Mark where leukocytes are.
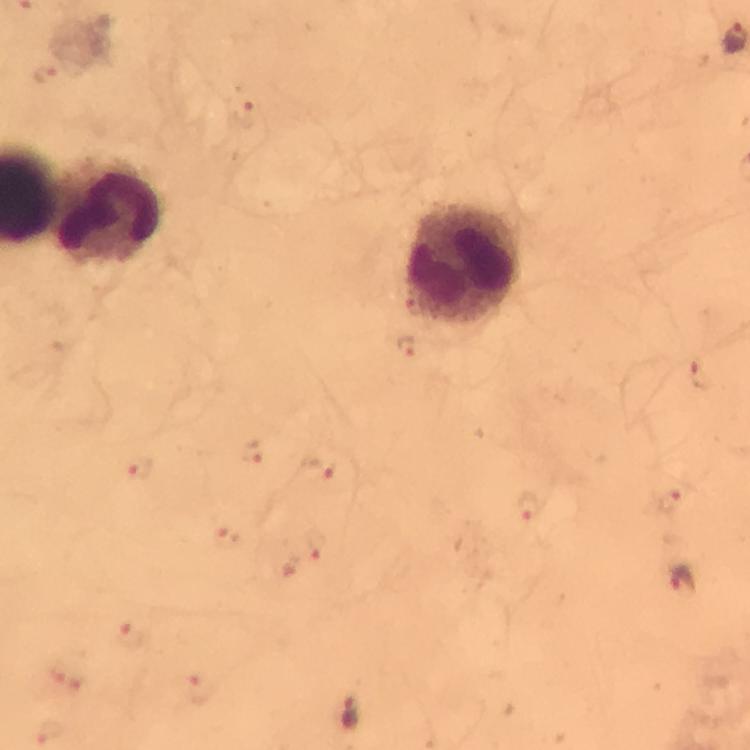
Approximate centers as {x, y} in pixels.
Leukocytes: {107, 211}, {466, 261}.

Malaria parasite locations: {47, 72}, {242, 114}, {406, 345}, {700, 375}, {253, 454}, {318, 469}, {139, 472}, {670, 502}, {528, 507}, {226, 537}, {317, 545}, {685, 580}, {131, 635}, {200, 689}, {351, 713}, {52, 732}. From a malaria diagnostic workup. Photographed through the microscope with a smartphone camera. Image is 750×750 pixels. 100x magnification. Thick blood film. Immersion oil was used. Cropped region of a single field of view. Giemsa-stained preparation.